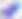

Toxoplasma gondii is seen. 400x magnification. Photomicrograph.